Give the position of every leukocyte visible.
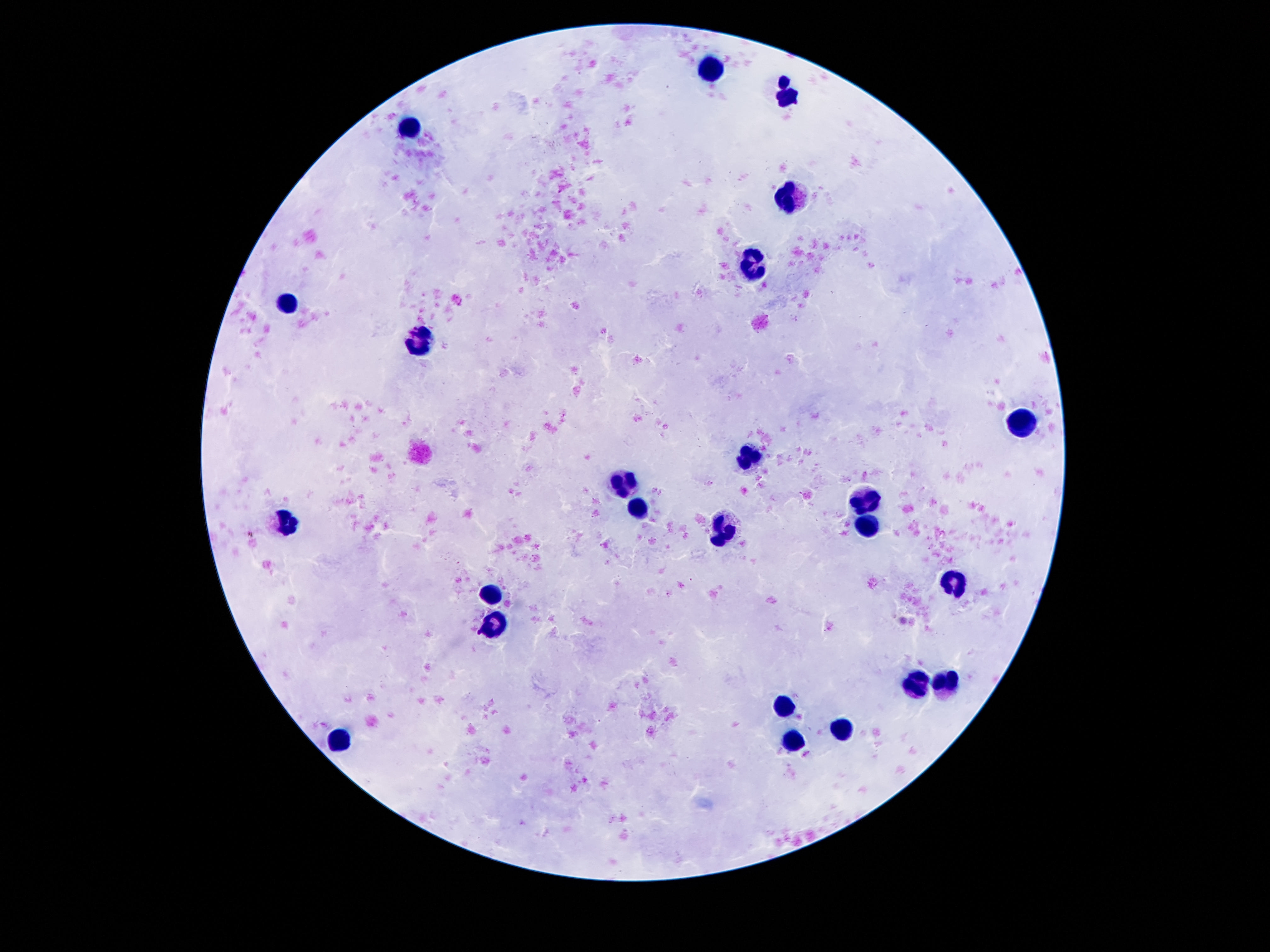
Approximate object centers, in pixels from the top-left corner.
Leukocytes: (x=712, y=66), (x=785, y=95), (x=414, y=125), (x=787, y=195), (x=752, y=266), (x=290, y=303), (x=418, y=339), (x=1022, y=420), (x=749, y=459), (x=621, y=482), (x=867, y=496), (x=639, y=509), (x=288, y=524), (x=865, y=527), (x=493, y=591), (x=495, y=624), (x=920, y=683), (x=948, y=684), (x=785, y=706), (x=844, y=729), (x=794, y=740), (x=345, y=741).

preparation = thick peripheral-blood smear
stain = Giemsa
magnification = 100x
field of view = one from this slide
image size = 1270×952 pixels
patient malaria status = not infected
capture = smartphone camera through the microscope eyepiece